Report the malaria status of this cell.
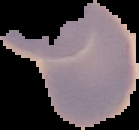
It is uninfected.

image type = cell region segmented out of the field of view; surrounding area masked to black
preparation = thin blood film
image size = 139×130 pixels